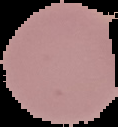 The area outside the segmented cell region is set to black. Result: no Plasmodium parasites seen. Image is 118×127 pixels. From a thin blood smear.